Outline each blood parasite and name the species.
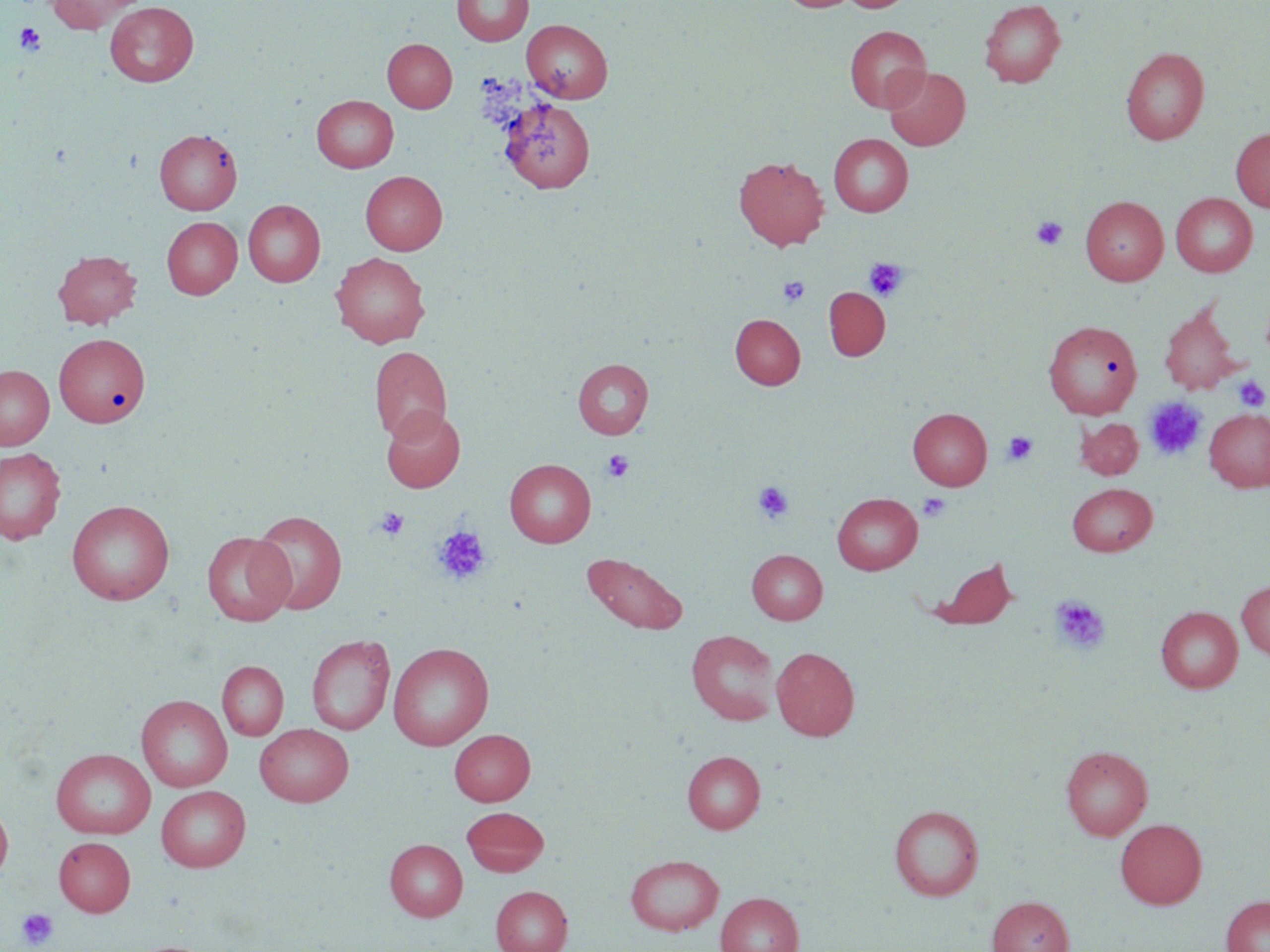
No blood parasites observed.

Approximate bounding boxes as (x1, y1, x2, y2) in pixels. Platelet locations: (15, 22, 47, 55), (1031, 217, 1067, 249), (864, 258, 909, 301), (778, 276, 810, 307), (1233, 375, 1268, 412), (1144, 396, 1207, 461), (1002, 431, 1038, 467), (602, 449, 635, 482), (753, 481, 795, 524), (918, 493, 950, 522), (374, 507, 409, 541), (433, 526, 491, 585), (1050, 596, 1110, 653), (18, 907, 59, 950). Uninfected red blood cell locations: (46, 0, 143, 33), (452, 0, 533, 46), (778, 0, 859, 12), (841, 0, 913, 12), (979, 0, 1066, 88), (105, 2, 199, 87), (522, 19, 612, 103), (844, 26, 930, 113), (383, 38, 457, 113), (1120, 47, 1209, 145), (883, 67, 970, 150), (312, 95, 398, 172), (497, 96, 597, 194), (1231, 127, 1270, 212), (154, 128, 242, 214), (829, 134, 913, 216), (734, 155, 829, 250), (360, 171, 447, 255), (1171, 192, 1257, 277), (1080, 195, 1168, 285), (243, 200, 325, 287), (162, 217, 242, 299), (53, 249, 142, 329), (331, 252, 430, 347), (823, 287, 890, 360), (1159, 303, 1240, 395), (730, 314, 805, 389), (1043, 320, 1141, 419), (54, 334, 150, 427), (369, 345, 452, 443), (572, 358, 653, 439), (0, 365, 53, 450), (380, 406, 464, 493), (908, 407, 992, 490), (1204, 408, 1270, 492), (1076, 417, 1143, 479), (0, 448, 66, 544), (505, 459, 596, 547), (1067, 482, 1157, 556), (832, 492, 923, 575), (67, 499, 175, 605), (251, 509, 347, 614), (202, 531, 295, 626), (747, 549, 827, 624), (581, 551, 689, 635), (926, 555, 1019, 631), (1236, 580, 1270, 661), (1155, 606, 1243, 693), (686, 629, 780, 725), (306, 634, 396, 736), (388, 643, 494, 750), (771, 647, 859, 740), (217, 661, 288, 741), (136, 695, 232, 792), (254, 724, 354, 806), (450, 729, 535, 805), (1061, 745, 1152, 841), (51, 749, 156, 839), (682, 750, 765, 833), (156, 785, 250, 872), (0, 798, 13, 883), (889, 804, 984, 901), (461, 806, 549, 876), (1115, 818, 1207, 909), (54, 837, 135, 916), (385, 839, 467, 921), (625, 854, 724, 935), (490, 886, 572, 952), (716, 892, 803, 952), (987, 896, 1074, 952), (1221, 896, 1270, 952). Slide-level diagnosis: no evidence of blood parasites. Image is 1270×952 pixels. Optical microscopy. Captured at 1000x magnification. One field of a larger specimen. Thin blood film. May-Grünwald-Giemsa-stained preparation.